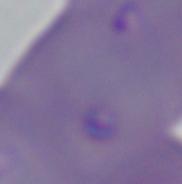
Summary:
  - Magnification: 1000x
  - Identification: Babesia
  - Modality: photomicrograph